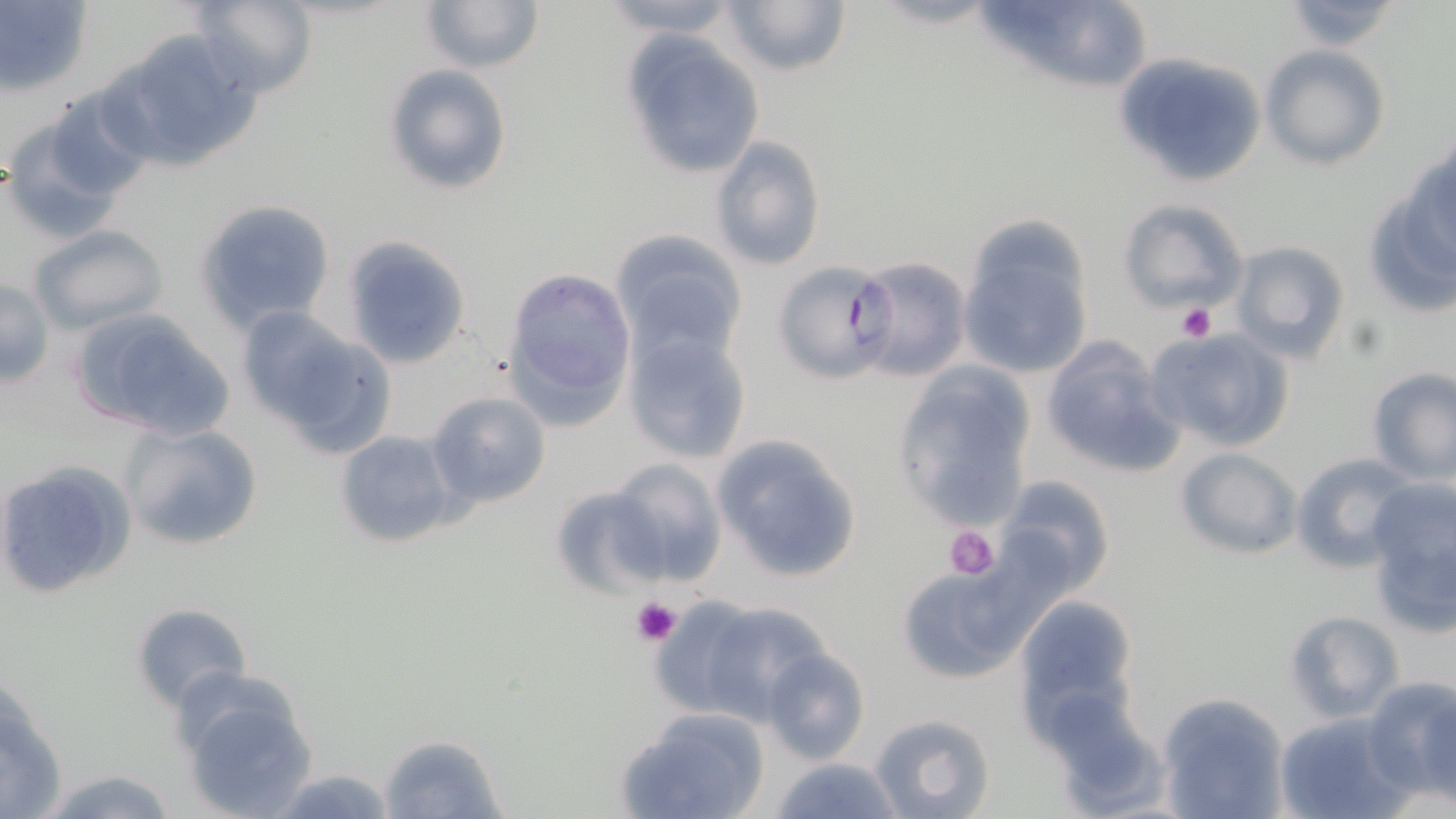

Approximate bounding boxes as named x1/y1/x2/y2 corners in pixels. Platelet locations: (x1=1176, y1=301, x2=1217, y2=342), (x1=946, y1=526, x2=1001, y2=579), (x1=632, y1=598, x2=681, y2=647). Uninfected red blood cell locations: (x1=188, y1=0, x2=317, y2=96), (x1=419, y1=0, x2=544, y2=75), (x1=597, y1=0, x2=744, y2=39), (x1=722, y1=0, x2=851, y2=78), (x1=1019, y1=1, x2=1149, y2=105), (x1=1283, y1=2, x2=1403, y2=50), (x1=111, y1=29, x2=266, y2=168), (x1=619, y1=31, x2=766, y2=181), (x1=1261, y1=46, x2=1389, y2=169), (x1=1114, y1=51, x2=1267, y2=187), (x1=383, y1=64, x2=512, y2=196), (x1=43, y1=84, x2=154, y2=200), (x1=2, y1=118, x2=126, y2=240), (x1=710, y1=135, x2=827, y2=271), (x1=1358, y1=165, x2=1456, y2=322), (x1=1118, y1=198, x2=1250, y2=314), (x1=194, y1=199, x2=336, y2=332), (x1=28, y1=224, x2=167, y2=332), (x1=957, y1=225, x2=1095, y2=382), (x1=608, y1=229, x2=747, y2=363), (x1=344, y1=236, x2=471, y2=370), (x1=1227, y1=239, x2=1352, y2=366), (x1=771, y1=260, x2=897, y2=385), (x1=504, y1=267, x2=637, y2=423), (x1=0, y1=276, x2=53, y2=390), (x1=234, y1=305, x2=376, y2=440), (x1=67, y1=307, x2=237, y2=443), (x1=621, y1=328, x2=753, y2=463), (x1=1147, y1=328, x2=1295, y2=456), (x1=1041, y1=337, x2=1184, y2=478), (x1=891, y1=363, x2=1037, y2=532), (x1=1365, y1=366, x2=1456, y2=485), (x1=427, y1=389, x2=552, y2=508), (x1=118, y1=421, x2=264, y2=551), (x1=333, y1=428, x2=459, y2=548), (x1=709, y1=432, x2=864, y2=583), (x1=1174, y1=447, x2=1302, y2=561), (x1=1290, y1=452, x2=1421, y2=573), (x1=605, y1=459, x2=727, y2=585), (x1=995, y1=474, x2=1116, y2=594), (x1=1362, y1=481, x2=1456, y2=635), (x1=550, y1=486, x2=672, y2=596), (x1=892, y1=565, x2=1032, y2=682), (x1=652, y1=589, x2=835, y2=727), (x1=1012, y1=597, x2=1141, y2=736), (x1=131, y1=601, x2=252, y2=711), (x1=1284, y1=612, x2=1406, y2=724), (x1=761, y1=648, x2=872, y2=764), (x1=170, y1=675, x2=322, y2=818), (x1=0, y1=676, x2=69, y2=819), (x1=1364, y1=676, x2=1456, y2=801), (x1=1159, y1=693, x2=1290, y2=818), (x1=1043, y1=694, x2=1171, y2=815), (x1=615, y1=706, x2=770, y2=819), (x1=1275, y1=711, x2=1410, y2=819), (x1=871, y1=712, x2=996, y2=819), (x1=377, y1=731, x2=507, y2=818), (x1=770, y1=756, x2=901, y2=818), (x1=34, y1=764, x2=181, y2=819), (x1=266, y1=767, x2=400, y2=819). Plasmodium falciparum-infected red blood cell locations: (x1=852, y1=256, x2=971, y2=382). Slide-level diagnosis: Plasmodium falciparum. Image is 1456×819 pixels. May-Grünwald-Giemsa stain. 1000x magnification. Thin blood smear. Optical microscopy. Single field of view.